Locate every Plasmodium falciparum-infected red blood cell.
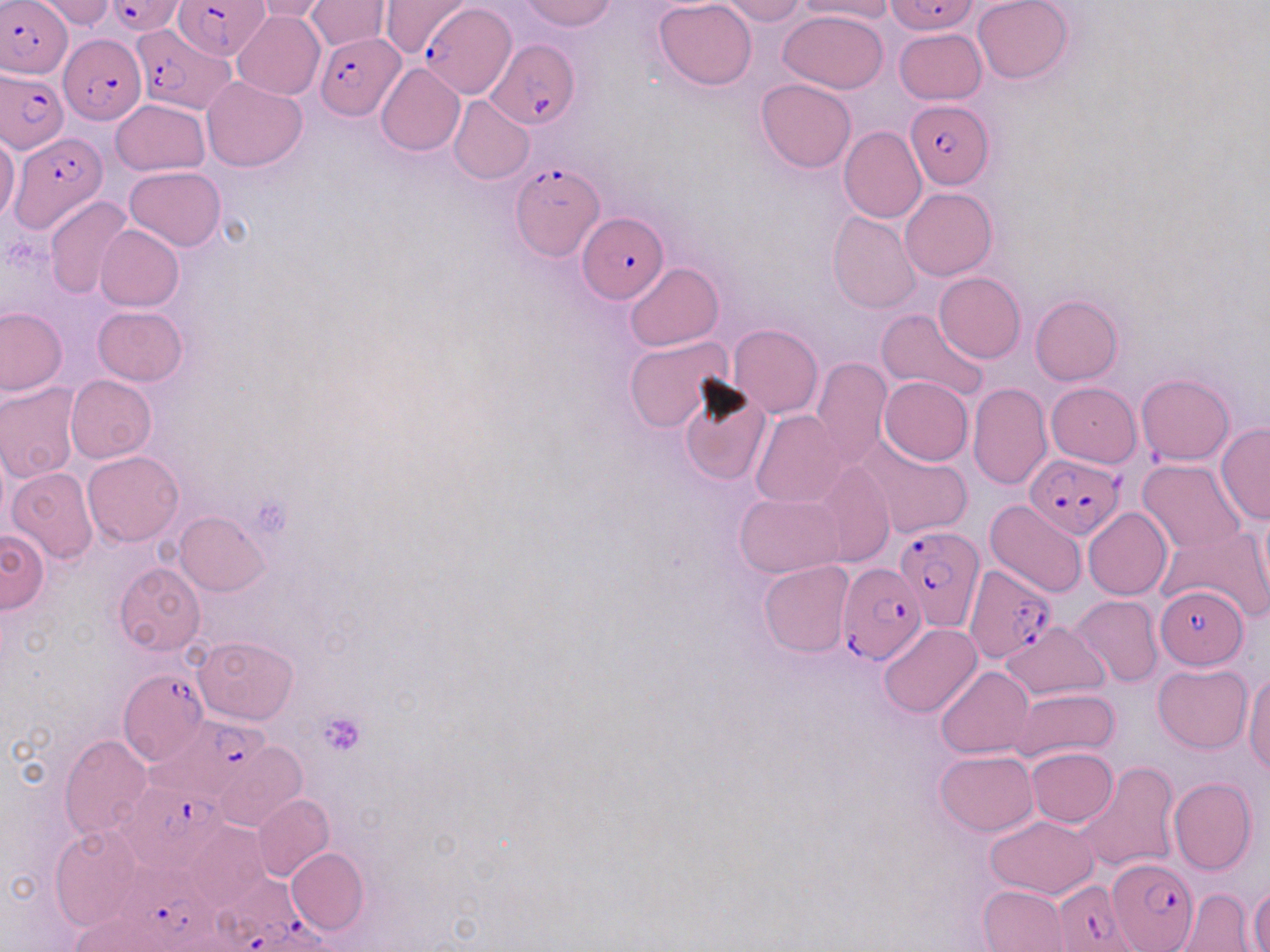

Approximate bounding boxes as named x1/y1/x2/y2 corners in pixels.
Plasmodium falciparum-infected red blood cells: (x1=1, y1=0, x2=73, y2=79), (x1=106, y1=0, x2=186, y2=36), (x1=174, y1=0, x2=267, y2=59), (x1=886, y1=0, x2=978, y2=35), (x1=422, y1=4, x2=517, y2=97), (x1=129, y1=28, x2=232, y2=116), (x1=313, y1=33, x2=405, y2=118), (x1=58, y1=35, x2=147, y2=124), (x1=486, y1=39, x2=579, y2=131), (x1=0, y1=68, x2=71, y2=154), (x1=904, y1=100, x2=993, y2=187), (x1=11, y1=133, x2=103, y2=228), (x1=510, y1=161, x2=603, y2=259), (x1=578, y1=216, x2=666, y2=303), (x1=1024, y1=455, x2=1122, y2=538), (x1=895, y1=524, x2=982, y2=632), (x1=838, y1=563, x2=924, y2=665), (x1=964, y1=564, x2=1058, y2=661), (x1=1155, y1=585, x2=1248, y2=668), (x1=117, y1=666, x2=208, y2=767), (x1=139, y1=719, x2=276, y2=806), (x1=119, y1=781, x2=232, y2=871), (x1=1107, y1=857, x2=1198, y2=951), (x1=122, y1=862, x2=221, y2=952), (x1=207, y1=875, x2=336, y2=952), (x1=1051, y1=880, x2=1136, y2=952).

slide-level diagnosis = Plasmodium falciparum
preparation = thin blood film
platelet locations = approximate bounding boxes as named x1/y1/x2/y2 corners in pixels: (x1=254, y1=495, x2=292, y2=535), (x1=319, y1=711, x2=367, y2=757)
modality = optical microscopy
image size = 1270×952 pixels
uninfected red blood cell locations = approximate bounding boxes as named x1/y1/x2/y2 corners in pixels: (x1=33, y1=0, x2=118, y2=30), (x1=378, y1=0, x2=473, y2=57), (x1=520, y1=0, x2=617, y2=31), (x1=654, y1=0, x2=757, y2=89), (x1=719, y1=0, x2=807, y2=24), (x1=797, y1=0, x2=897, y2=21), (x1=972, y1=0, x2=1074, y2=85), (x1=249, y1=1, x2=337, y2=23), (x1=305, y1=1, x2=389, y2=52), (x1=779, y1=9, x2=890, y2=93), (x1=233, y1=11, x2=324, y2=99), (x1=894, y1=29, x2=986, y2=105), (x1=375, y1=63, x2=465, y2=155), (x1=201, y1=76, x2=309, y2=171), (x1=754, y1=78, x2=855, y2=172), (x1=448, y1=95, x2=535, y2=185), (x1=111, y1=99, x2=209, y2=176), (x1=839, y1=126, x2=926, y2=224), (x1=0, y1=134, x2=21, y2=224), (x1=124, y1=165, x2=225, y2=250), (x1=900, y1=187, x2=998, y2=280), (x1=44, y1=195, x2=134, y2=299), (x1=827, y1=211, x2=922, y2=313), (x1=96, y1=224, x2=184, y2=311), (x1=625, y1=263, x2=723, y2=350), (x1=934, y1=272, x2=1026, y2=362), (x1=1030, y1=296, x2=1122, y2=384), (x1=0, y1=305, x2=67, y2=395), (x1=92, y1=306, x2=187, y2=386), (x1=877, y1=309, x2=987, y2=404), (x1=728, y1=324, x2=822, y2=419), (x1=625, y1=337, x2=733, y2=433), (x1=811, y1=357, x2=891, y2=469), (x1=1135, y1=373, x2=1234, y2=465), (x1=66, y1=375, x2=156, y2=462), (x1=677, y1=375, x2=772, y2=484), (x1=879, y1=376, x2=972, y2=465), (x1=0, y1=381, x2=82, y2=482), (x1=968, y1=382, x2=1052, y2=489), (x1=1046, y1=382, x2=1141, y2=467), (x1=751, y1=409, x2=847, y2=507), (x1=1215, y1=423, x2=1270, y2=524), (x1=854, y1=435, x2=972, y2=541), (x1=83, y1=450, x2=184, y2=545), (x1=813, y1=460, x2=895, y2=567), (x1=1138, y1=460, x2=1247, y2=554), (x1=7, y1=466, x2=98, y2=565), (x1=734, y1=493, x2=844, y2=578), (x1=1254, y1=500, x2=1269, y2=611), (x1=986, y1=501, x2=1088, y2=598), (x1=1083, y1=508, x2=1172, y2=599), (x1=175, y1=511, x2=270, y2=595), (x1=0, y1=526, x2=51, y2=612), (x1=1159, y1=526, x2=1270, y2=622), (x1=113, y1=561, x2=206, y2=657), (x1=758, y1=561, x2=853, y2=656), (x1=1072, y1=594, x2=1163, y2=687), (x1=997, y1=621, x2=1110, y2=701), (x1=878, y1=623, x2=982, y2=718), (x1=194, y1=635, x2=299, y2=723), (x1=1153, y1=663, x2=1252, y2=754), (x1=936, y1=666, x2=1034, y2=758), (x1=1244, y1=669, x2=1270, y2=775), (x1=1013, y1=688, x2=1120, y2=763), (x1=59, y1=734, x2=153, y2=838), (x1=213, y1=740, x2=307, y2=831), (x1=1026, y1=747, x2=1117, y2=827), (x1=935, y1=750, x2=1037, y2=835), (x1=1077, y1=762, x2=1179, y2=871), (x1=1168, y1=777, x2=1256, y2=876), (x1=252, y1=794, x2=334, y2=882), (x1=190, y1=807, x2=338, y2=895), (x1=986, y1=816, x2=1099, y2=900), (x1=183, y1=821, x2=271, y2=910), (x1=49, y1=823, x2=146, y2=932), (x1=286, y1=848, x2=368, y2=935), (x1=1248, y1=882, x2=1270, y2=950), (x1=979, y1=885, x2=1067, y2=951), (x1=1178, y1=888, x2=1253, y2=951), (x1=68, y1=909, x2=193, y2=952)
magnification = 1000x
field of view = single
stain = May-Grünwald-Giemsa